Evaluate for Plasmodium parasites.
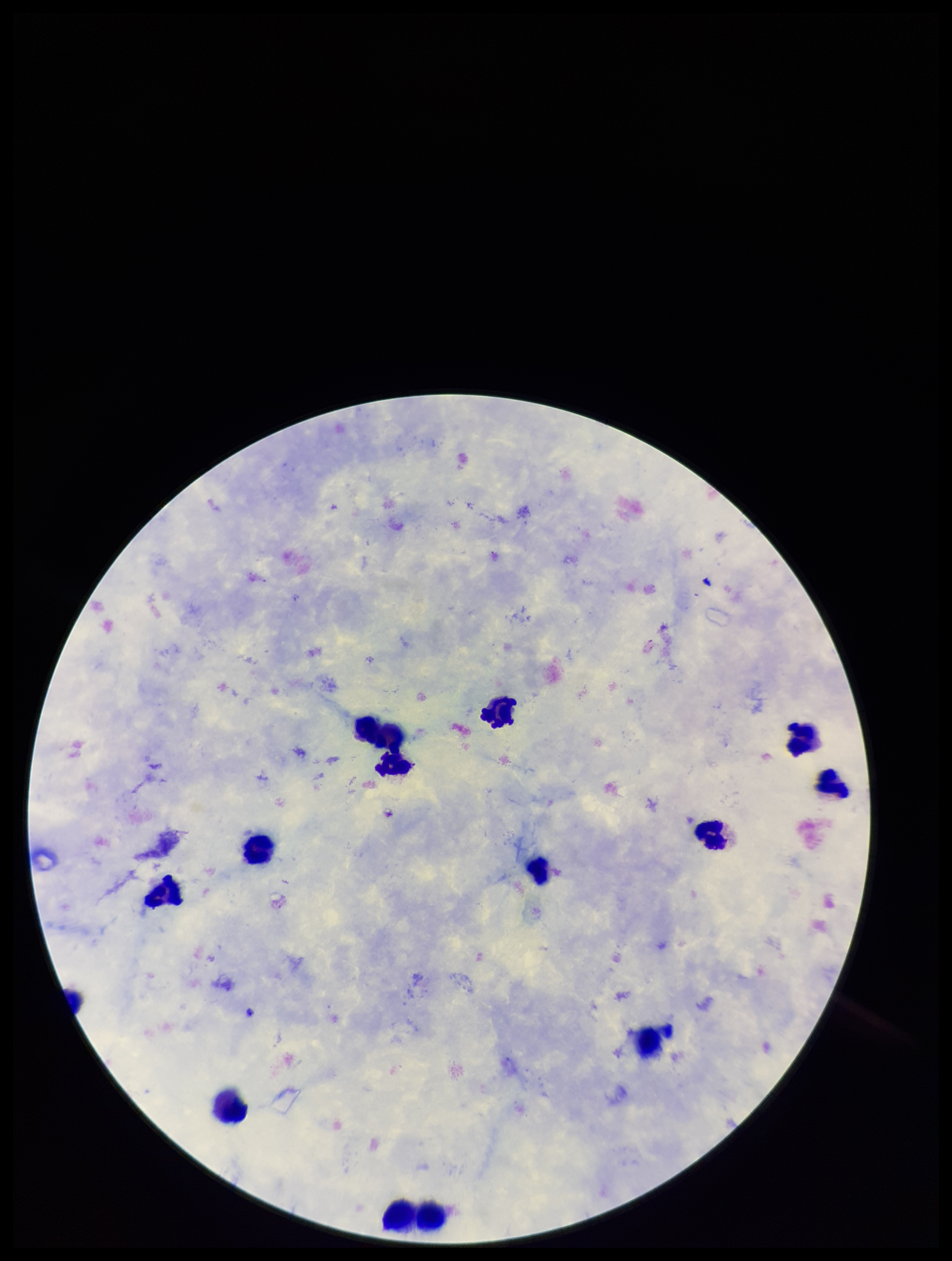
None seen.

Patient malaria status: infected. Smartphone photograph taken through the eyepiece of a microscope. Parasite count: 0. Image is 952×1261 pixels. Preparation: thick smear. Leukocyte count: 12. Species reported for this patient: Plasmodium falciparum. Stained with Giemsa. Single field of view.